Find the red blood cells that are infected with Plasmodium falciparum, and any of indeterminate infection status.
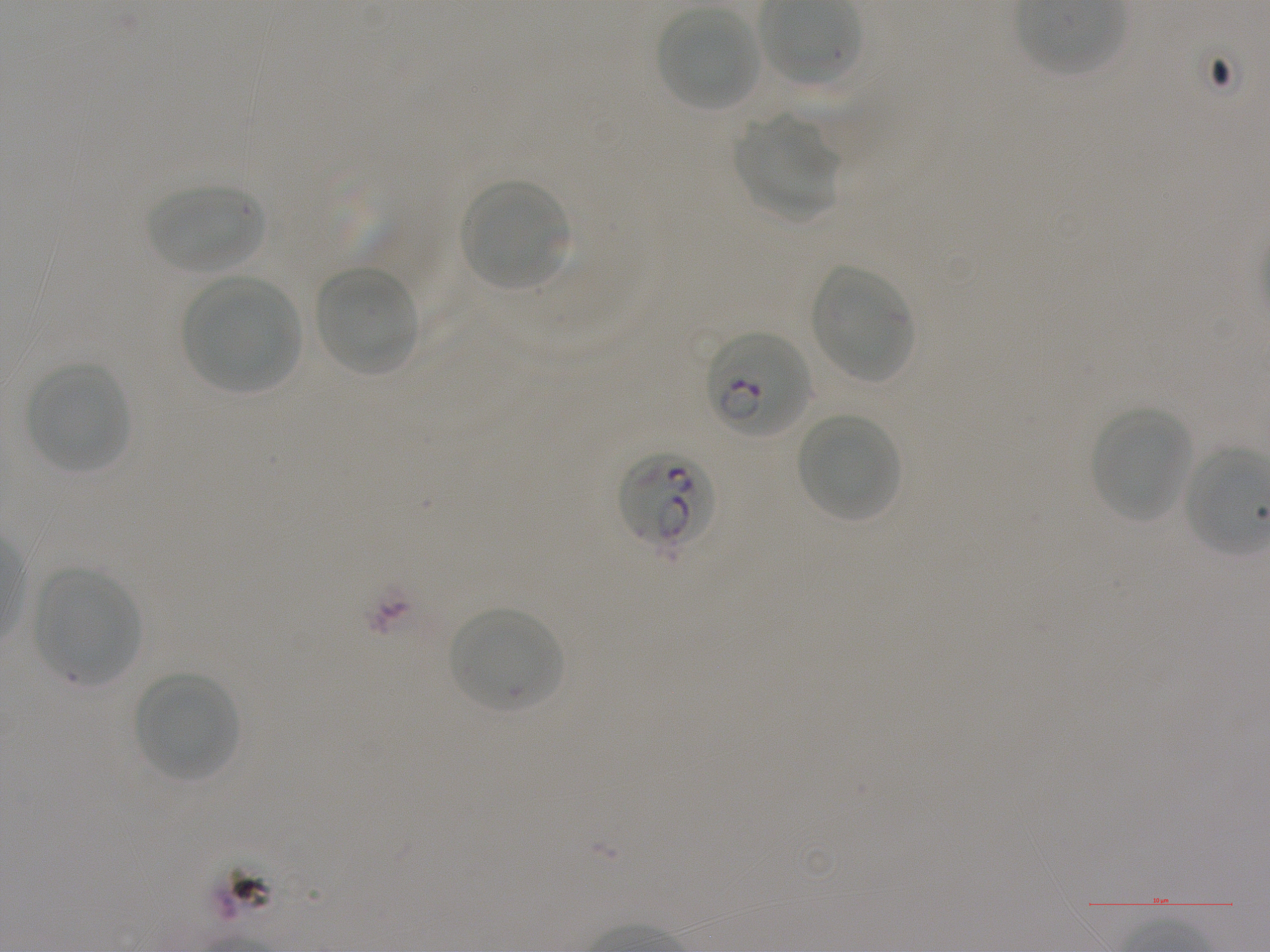
Approximate bounding boxes as [x1, y1, x2, y2] in pixels. Not every red blood cell is marked. A life-cycle stage — or a range of stages, where the recorded stages span more than one — follows each staged infected red blood cell.
Infected red blood cells: [707, 331, 811, 438] early ring to early trophozoite; [617, 451, 717, 556].
No red blood cells of indeterminate infection status observed.

Locations of uninfected red blood cells: [657, 8, 759, 112], [734, 116, 840, 224], [460, 179, 572, 290], [148, 184, 263, 274], [812, 264, 916, 383], [315, 266, 422, 375], [182, 276, 301, 393], [26, 363, 132, 474], [1090, 407, 1192, 522], [797, 413, 900, 523], [33, 568, 140, 687], [448, 606, 564, 714], [135, 672, 239, 781]. Blood group of the donor: A+. One field from this slide. Static in-vitro culture of Plasmodium falciparum strain NF54. Oil immersion, 100x objective (numerical aperture 1.25). Thin blood film. Image is 1270×952 pixels. Giemsa stain.